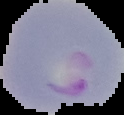
Result: Plasmodium parasites identified. From a thin blood film. Image is 124×115 pixels. The area outside the segmented cell region is set to black.